Assess this cell for malaria.
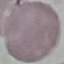
It is uninfected.

Summary:
  - Preparation: thin smear
  - Image type: automatically extracted cell patch, resized to 64 × 64 pixels
  - Stain: Giemsa
  - Capture: smartphone camera at the microscope eyepiece